Evaluate for Plasmodium parasites.
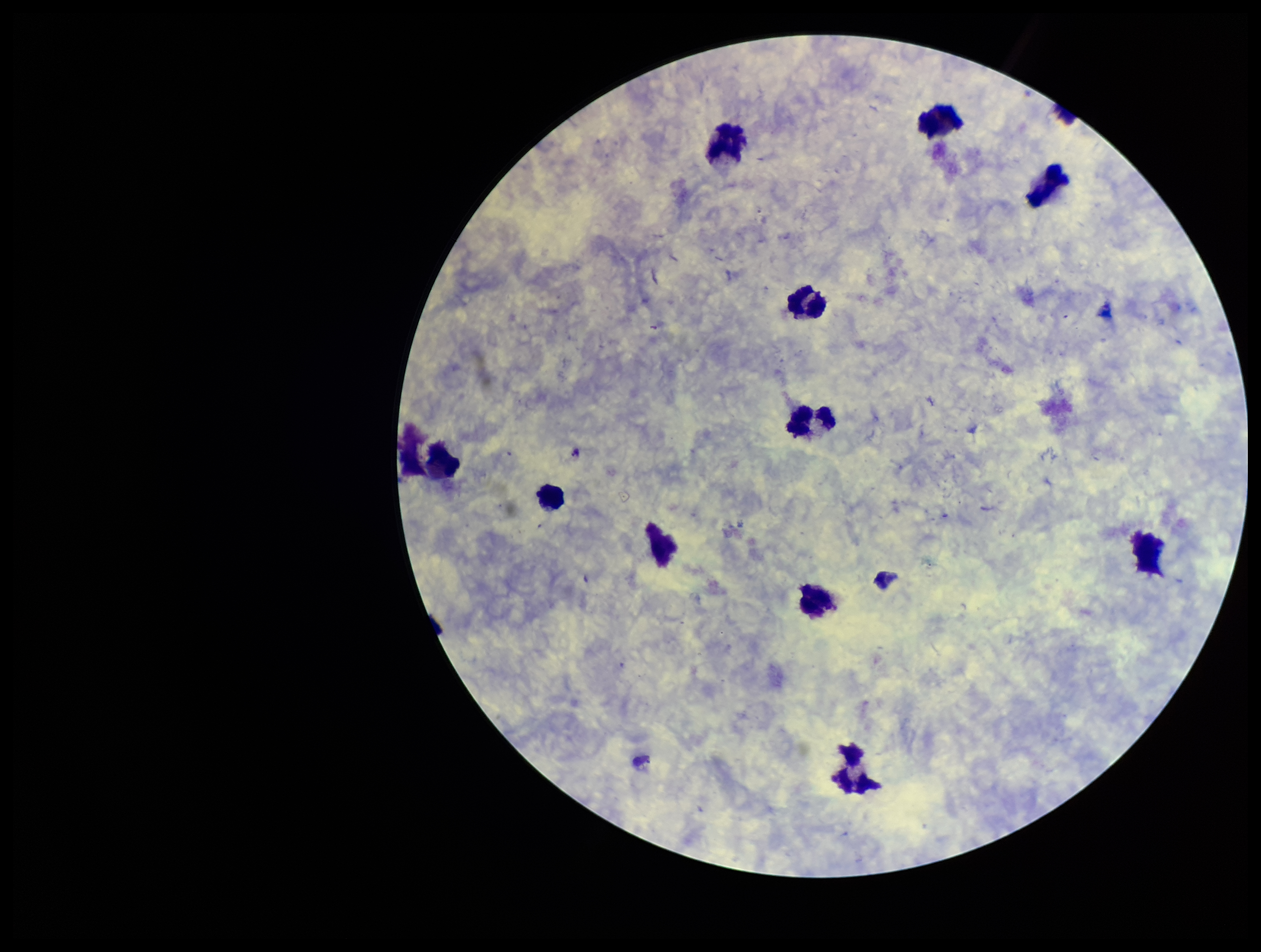
None detected.

{
  "parasite_count": 0,
  "patient_malaria_status": "negative",
  "capture": "smartphone photograph through the microscope eyepiece",
  "field_of_view": "one from this slide",
  "leukocyte_count": 11,
  "image_size": "1261×952 pixels",
  "preparation": "thick smear",
  "stain": "Giemsa"
}